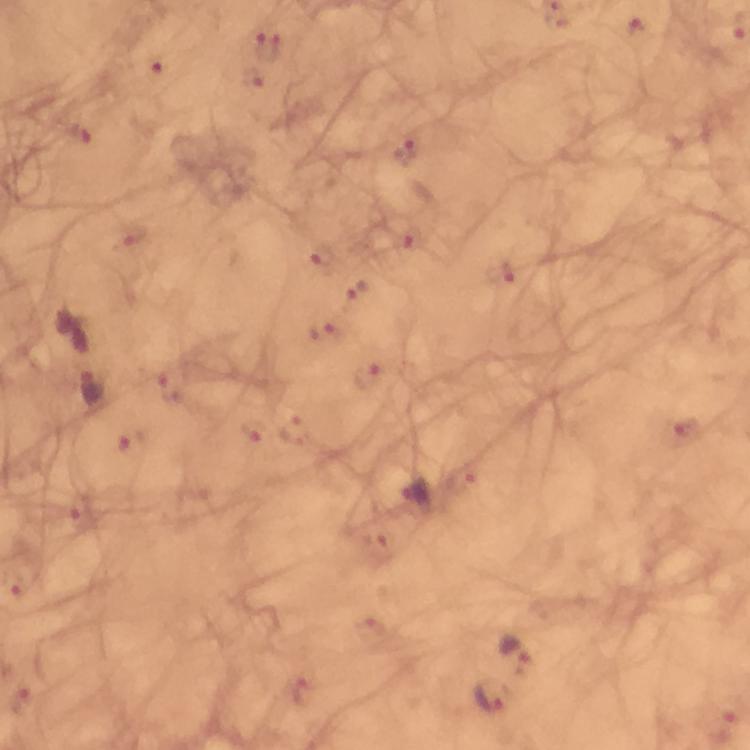
Approximate object centers, in pixels from the top-left corner. Malaria parasite locations: (x=636, y=30), (x=268, y=41), (x=152, y=68), (x=251, y=77), (x=78, y=133), (x=407, y=150), (x=131, y=233), (x=412, y=240), (x=321, y=253), (x=500, y=273), (x=357, y=289), (x=322, y=329), (x=367, y=374), (x=170, y=387), (x=95, y=388), (x=683, y=428), (x=293, y=431), (x=252, y=433), (x=130, y=442), (x=460, y=479), (x=79, y=521), (x=375, y=544), (x=369, y=630), (x=515, y=647), (x=300, y=690), (x=491, y=700), (x=21, y=702). Image is 750×750 pixels. Cropped region of a single field of view. At 100x magnification. Immersion oil was used. Thick smear. Photographed with a smartphone mounted on the microscope. Giemsa stain. From a malaria diagnostic workup.